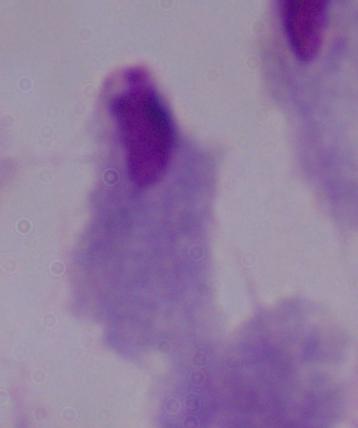 Photomicrograph. Captured at 1000x magnification. A trichomonad is seen.